State which parasite is depicted.
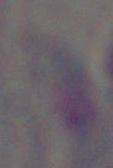

Toxoplasma gondii.

Captured at 1000x magnification. Photomicrograph.